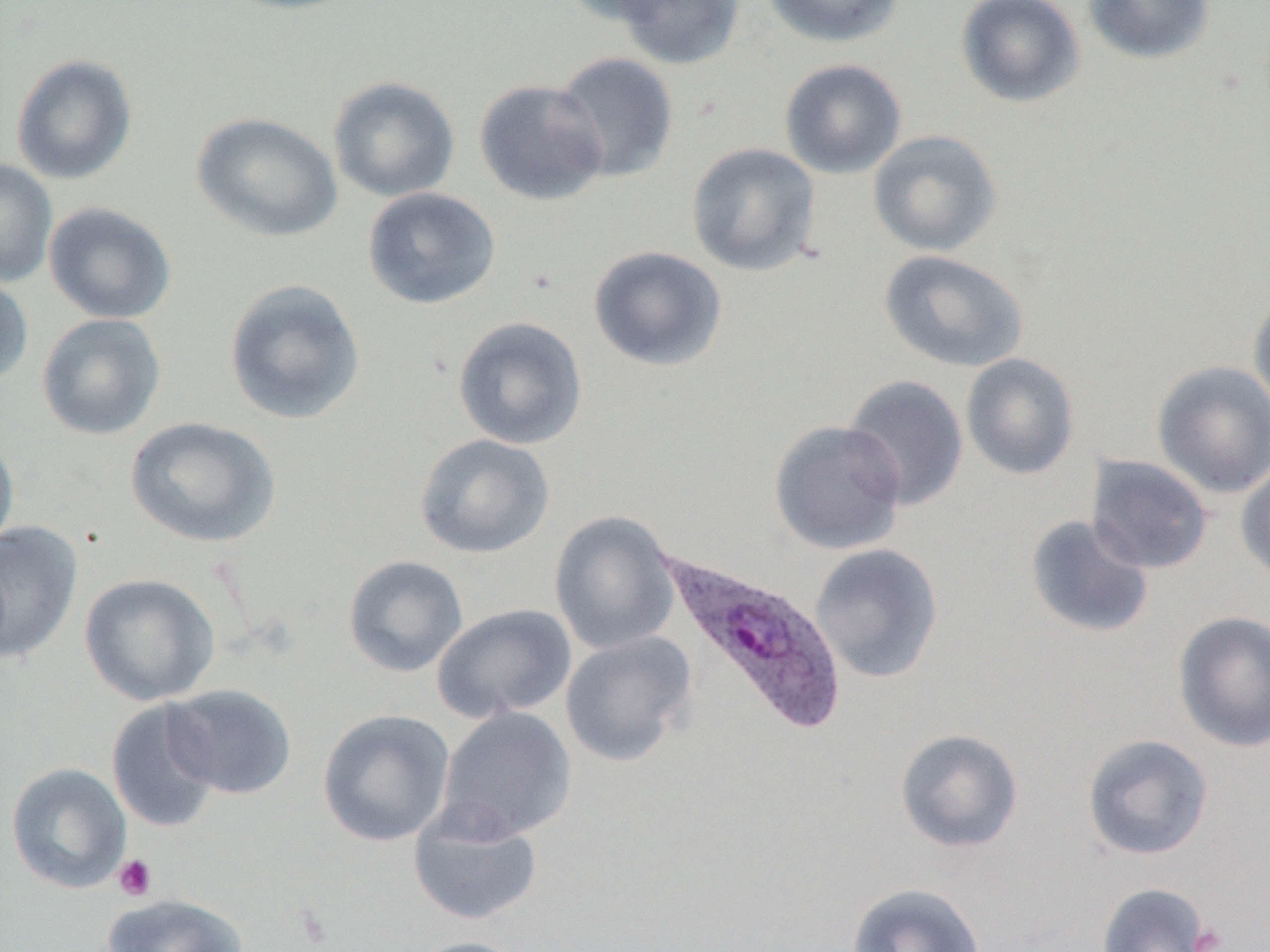

Summary:
  - Coordinate format: approximate bounding boxes as (x1, y1, x2, y2) in pixels
  - Platelet locations: (113, 854, 158, 901), (1190, 924, 1229, 952)
  - Uninfected red blood cell locations: (216, 0, 368, 16), (556, 0, 684, 25), (613, 0, 746, 69), (760, 0, 905, 48), (955, 0, 1085, 108), (1083, 0, 1215, 65), (551, 51, 679, 183), (11, 54, 138, 186), (780, 58, 907, 179), (327, 75, 460, 203), (474, 78, 609, 206), (191, 111, 342, 242), (868, 129, 1003, 257), (686, 142, 822, 277), (0, 158, 58, 288), (362, 187, 501, 310), (44, 202, 177, 324), (588, 246, 728, 372), (879, 249, 1030, 374), (0, 272, 34, 388), (224, 279, 366, 425), (1247, 288, 1270, 424), (36, 313, 166, 441), (451, 316, 588, 450), (960, 352, 1081, 481), (1151, 360, 1270, 499), (842, 374, 969, 511), (126, 417, 281, 548), (768, 419, 907, 556), (0, 431, 19, 555), (414, 433, 554, 559), (1086, 455, 1213, 574), (1235, 460, 1270, 582), (549, 510, 682, 655), (1024, 514, 1154, 639), (0, 520, 83, 665), (809, 544, 944, 684), (343, 555, 469, 678), (79, 573, 220, 706), (432, 603, 577, 723), (1172, 610, 1270, 753), (560, 631, 697, 767), (163, 684, 297, 800), (106, 700, 222, 833), (435, 707, 578, 844), (317, 709, 455, 847), (894, 727, 1024, 854), (1081, 733, 1214, 861), (6, 762, 132, 894), (409, 806, 544, 926), (845, 882, 987, 952), (1095, 882, 1216, 952), (101, 893, 250, 952), (405, 935, 532, 952)
  - Plasmodium ovale-infected red blood cell locations: (654, 548, 848, 738)
  - Slide-level diagnosis: Plasmodium ovale
  - Modality: optical microscopy
  - Magnification: 1000x
  - Field of view: one of a larger specimen
  - Image size: 1270×952 pixels
  - Preparation: thin blood film